Locate and identify every blood parasite.
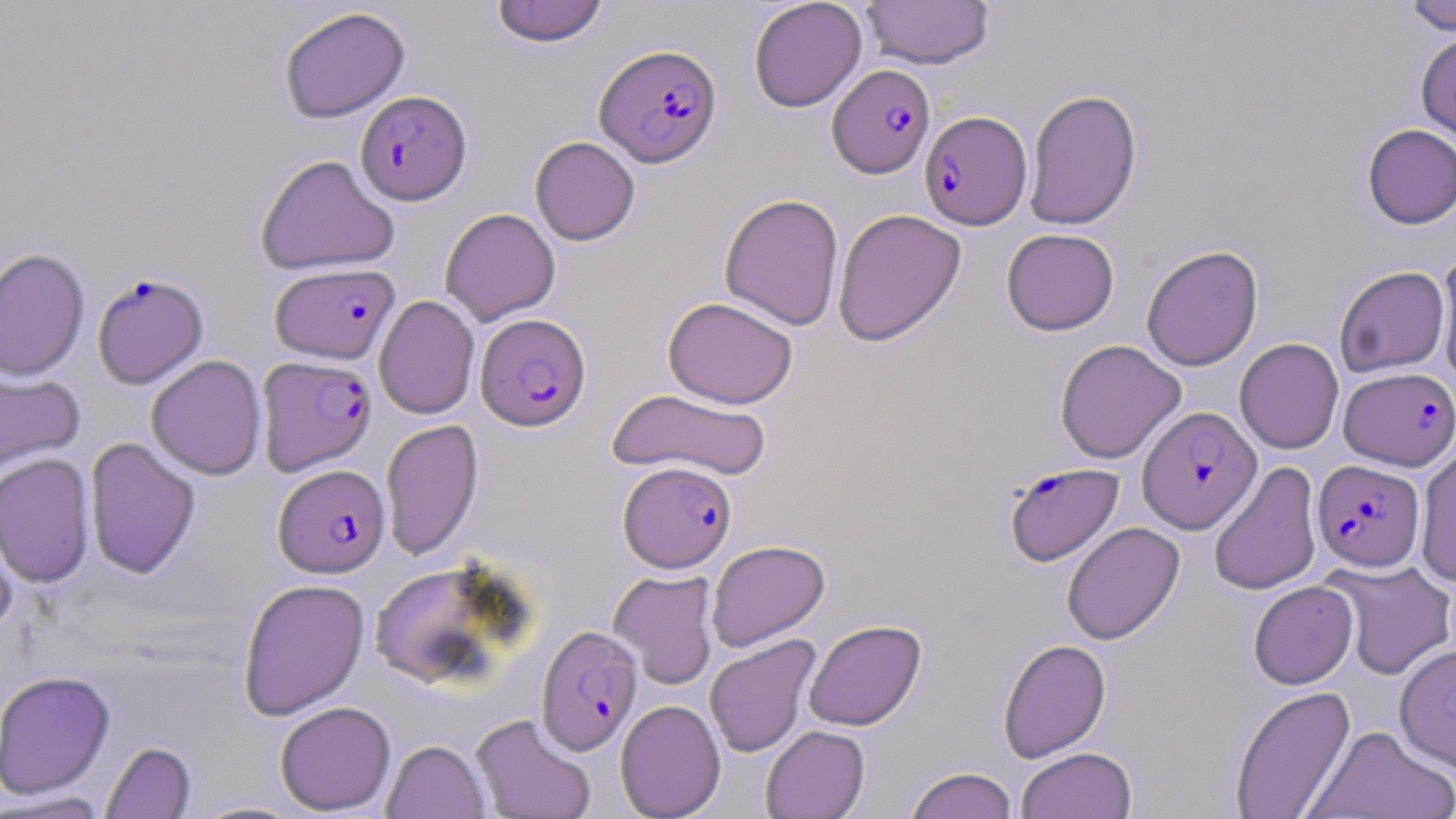
Approximate bounding boxes as (x1,y1)-(x2,y2) corner pairs in pixels.
Plasmodium falciparum-infected red blood cells: (595,43)-(722,167), (828,64)-(935,178), (355,91)-(471,204), (920,110)-(1032,229), (270,262)-(400,364), (92,272)-(208,389), (475,313)-(591,431), (256,355)-(377,475), (1339,367)-(1455,470), (1137,406)-(1261,534), (1313,459)-(1424,571), (618,461)-(736,573), (1004,462)-(1124,566), (273,463)-(390,578), (536,625)-(642,755).
No Plasmodium ovale, Plasmodium malariae, Plasmodium vivax, Babesia divergens, or Trypanosoma brucei observed.

Summary:
  - Uninfected red blood cell locations: (748,0)-(867,113), (861,0)-(994,69), (490,1)-(609,47), (1403,1)-(1456,34), (279,7)-(411,123), (1416,32)-(1456,145), (1024,88)-(1142,231), (1362,124)-(1456,229), (530,136)-(640,245), (255,154)-(400,276), (719,193)-(844,330), (440,208)-(561,326), (832,208)-(966,346), (1001,228)-(1119,335), (1141,245)-(1263,371), (0,248)-(90,381), (1436,251)-(1456,387), (1334,265)-(1450,377), (373,295)-(480,419), (663,296)-(798,408), (1234,338)-(1344,454), (1055,339)-(1186,464), (147,355)-(266,480), (0,365)-(85,481), (607,389)-(773,482), (381,419)-(483,560), (84,436)-(200,579), (1415,444)-(1456,587), (0,453)-(95,588), (1208,461)-(1322,595), (0,502)-(21,637), (1062,522)-(1184,645), (706,540)-(830,651), (1324,559)-(1456,681), (368,560)-(516,689), (608,570)-(719,689), (237,577)-(370,720), (1248,580)-(1358,689), (804,619)-(926,731), (704,635)-(821,758), (998,638)-(1111,763), (1395,643)-(1456,772), (0,670)-(115,799), (1229,685)-(1356,818), (615,700)-(726,818), (275,701)-(396,815), (471,713)-(596,819), (1305,724)-(1455,818), (760,725)-(870,819), (382,739)-(490,819), (100,740)-(196,818), (1015,746)-(1137,819), (905,767)-(1018,819), (1,791)-(110,818), (184,799)-(309,818)
  - Slide-level diagnosis: Plasmodium falciparum
  - Field of view: single
  - Preparation: thin blood smear
  - Modality: optical microscopy
  - Stain: May-Grünwald-Giemsa
  - Image size: 1456×819 pixels
  - Magnification: 1000x